Comment on the morphology of the erythrocytes.
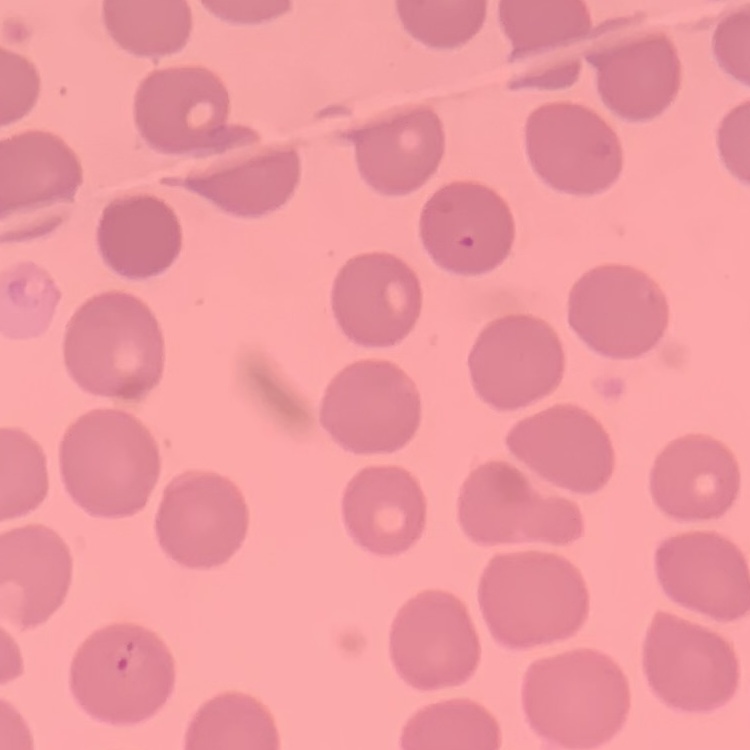
No rouleaux formation.

preparation = thin peripheral smear
stain = Field's or Giemsa
image type = one tile cut from a larger photomicrograph